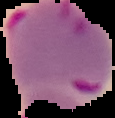

preparation = thin blood smear
result = malaria parasites identified
image size = 115×118 pixels
image type = cell region segmented out of the field of view; surrounding area masked to black